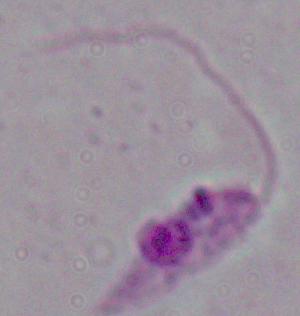

magnification = 1000x
modality = photomicrograph
identification = Leishmania